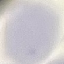

Malaria status: uninfected. Acquired by smartphone through the microscope eyepiece. Giemsa-stained preparation. Cell patch, automatically extracted from a larger field of view and resized to 64 × 64 pixels. Thin smear of blood.